Mark where platelets are.
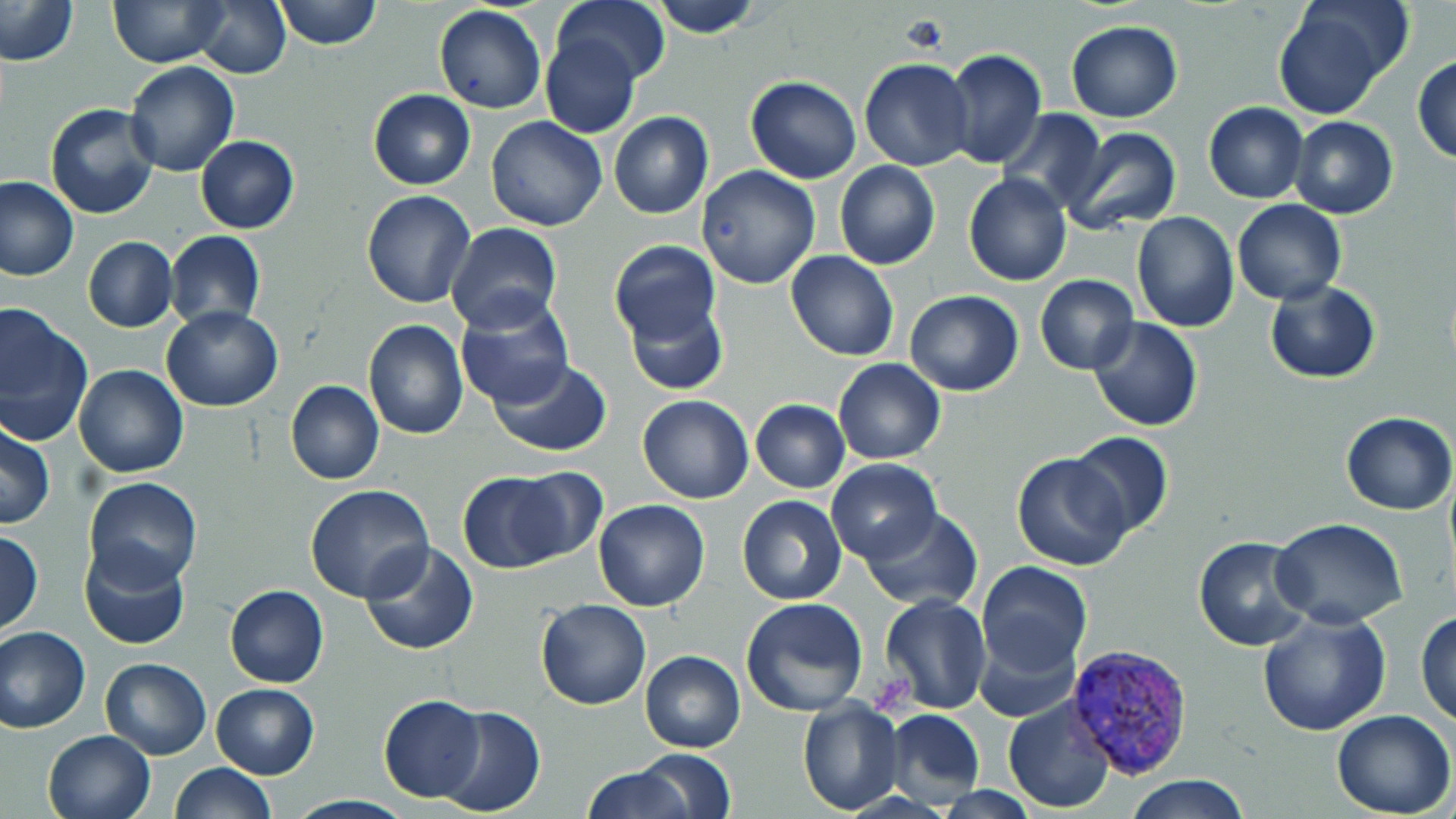
Approximate bounding boxes as named x1/y1/x2/y2 corners in pixels.
Platelets: (x1=898, y1=10, x2=951, y2=59), (x1=873, y1=673, x2=920, y2=713).

slide-level diagnosis = Plasmodium vivax
image size = 1456×819 pixels
stain = May-Grünwald-Giemsa
field of view = one of a larger specimen
magnification = 1000x
preparation = thin blood film
modality = light microscopy
uninfected red blood cell locations = approximate bounding boxes as named x1/y1/x2/y2 corners in pixels: (x1=0, y1=0, x2=79, y2=67), (x1=107, y1=0, x2=228, y2=67), (x1=191, y1=0, x2=291, y2=78), (x1=272, y1=0, x2=381, y2=49), (x1=552, y1=0, x2=667, y2=91), (x1=650, y1=0, x2=767, y2=37), (x1=1272, y1=2, x2=1408, y2=121), (x1=433, y1=4, x2=548, y2=115), (x1=1065, y1=21, x2=1182, y2=123), (x1=539, y1=31, x2=640, y2=139), (x1=942, y1=48, x2=1047, y2=168), (x1=1413, y1=54, x2=1456, y2=164), (x1=859, y1=57, x2=976, y2=171), (x1=123, y1=61, x2=240, y2=177), (x1=745, y1=76, x2=862, y2=184), (x1=367, y1=89, x2=475, y2=190), (x1=45, y1=102, x2=161, y2=219), (x1=1203, y1=103, x2=1309, y2=203), (x1=999, y1=109, x2=1109, y2=213), (x1=608, y1=112, x2=713, y2=220), (x1=485, y1=116, x2=607, y2=231), (x1=1289, y1=117, x2=1398, y2=219), (x1=1061, y1=127, x2=1182, y2=237), (x1=195, y1=136, x2=299, y2=234), (x1=835, y1=159, x2=940, y2=271), (x1=695, y1=165, x2=821, y2=289), (x1=964, y1=173, x2=1071, y2=287), (x1=0, y1=176, x2=78, y2=283), (x1=362, y1=191, x2=477, y2=309), (x1=1232, y1=199, x2=1346, y2=305), (x1=1131, y1=211, x2=1239, y2=330), (x1=444, y1=223, x2=562, y2=335), (x1=165, y1=231, x2=266, y2=329), (x1=82, y1=237, x2=176, y2=332), (x1=609, y1=241, x2=722, y2=352), (x1=786, y1=251, x2=898, y2=362), (x1=1036, y1=274, x2=1139, y2=375), (x1=1266, y1=280, x2=1382, y2=383), (x1=905, y1=290, x2=1025, y2=395), (x1=455, y1=292, x2=574, y2=411), (x1=622, y1=293, x2=728, y2=396), (x1=0, y1=304, x2=94, y2=446), (x1=162, y1=306, x2=283, y2=412), (x1=1088, y1=315, x2=1202, y2=430), (x1=362, y1=319, x2=468, y2=438), (x1=489, y1=358, x2=615, y2=457), (x1=833, y1=358, x2=945, y2=464), (x1=73, y1=364, x2=189, y2=478), (x1=752, y1=379, x2=935, y2=481), (x1=285, y1=381, x2=383, y2=485), (x1=637, y1=392, x2=754, y2=504), (x1=750, y1=400, x2=851, y2=492), (x1=1340, y1=412, x2=1455, y2=514), (x1=0, y1=422, x2=55, y2=530), (x1=1066, y1=432, x2=1173, y2=538), (x1=1011, y1=453, x2=1131, y2=572), (x1=826, y1=459, x2=941, y2=564), (x1=506, y1=468, x2=608, y2=563), (x1=457, y1=470, x2=570, y2=572), (x1=81, y1=477, x2=202, y2=591), (x1=304, y1=484, x2=434, y2=603), (x1=737, y1=495, x2=847, y2=606), (x1=592, y1=499, x2=710, y2=612), (x1=859, y1=507, x2=983, y2=610), (x1=1270, y1=518, x2=1407, y2=628), (x1=1, y1=530, x2=44, y2=632), (x1=1193, y1=536, x2=1311, y2=650), (x1=359, y1=541, x2=478, y2=656), (x1=78, y1=542, x2=191, y2=651), (x1=974, y1=561, x2=1091, y2=677), (x1=224, y1=585, x2=329, y2=687), (x1=879, y1=593, x2=992, y2=714), (x1=741, y1=597, x2=868, y2=718), (x1=536, y1=598, x2=650, y2=710), (x1=1255, y1=608, x2=1391, y2=737), (x1=1416, y1=610, x2=1455, y2=729), (x1=972, y1=623, x2=1080, y2=723), (x1=0, y1=625, x2=92, y2=734), (x1=638, y1=650, x2=746, y2=751), (x1=99, y1=657, x2=212, y2=759), (x1=211, y1=683, x2=319, y2=779), (x1=378, y1=695, x2=485, y2=802), (x1=1002, y1=695, x2=1116, y2=814), (x1=797, y1=697, x2=905, y2=814), (x1=435, y1=705, x2=545, y2=815), (x1=884, y1=708, x2=985, y2=805), (x1=1332, y1=709, x2=1454, y2=818), (x1=42, y1=729, x2=155, y2=819), (x1=635, y1=749, x2=736, y2=818), (x1=169, y1=762, x2=274, y2=818), (x1=582, y1=765, x2=693, y2=819), (x1=1123, y1=774, x2=1250, y2=818)
Plasmodium vivax-infected red blood cell locations = approximate bounding boxes as named x1/y1/x2/y2 corners in pixels: (x1=1067, y1=643, x2=1195, y2=780)